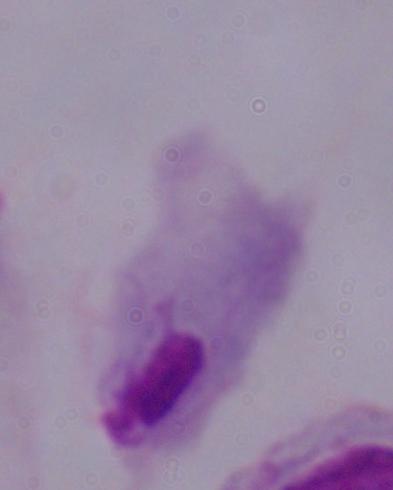
Summary:
  - Magnification: 1000x
  - Modality: micrograph
  - Identification: trichomonad